State which cell type is depicted.
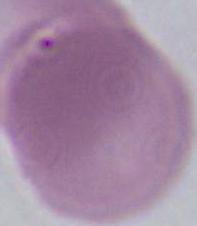

An erythrocyte.

1000x magnification. Micrograph.